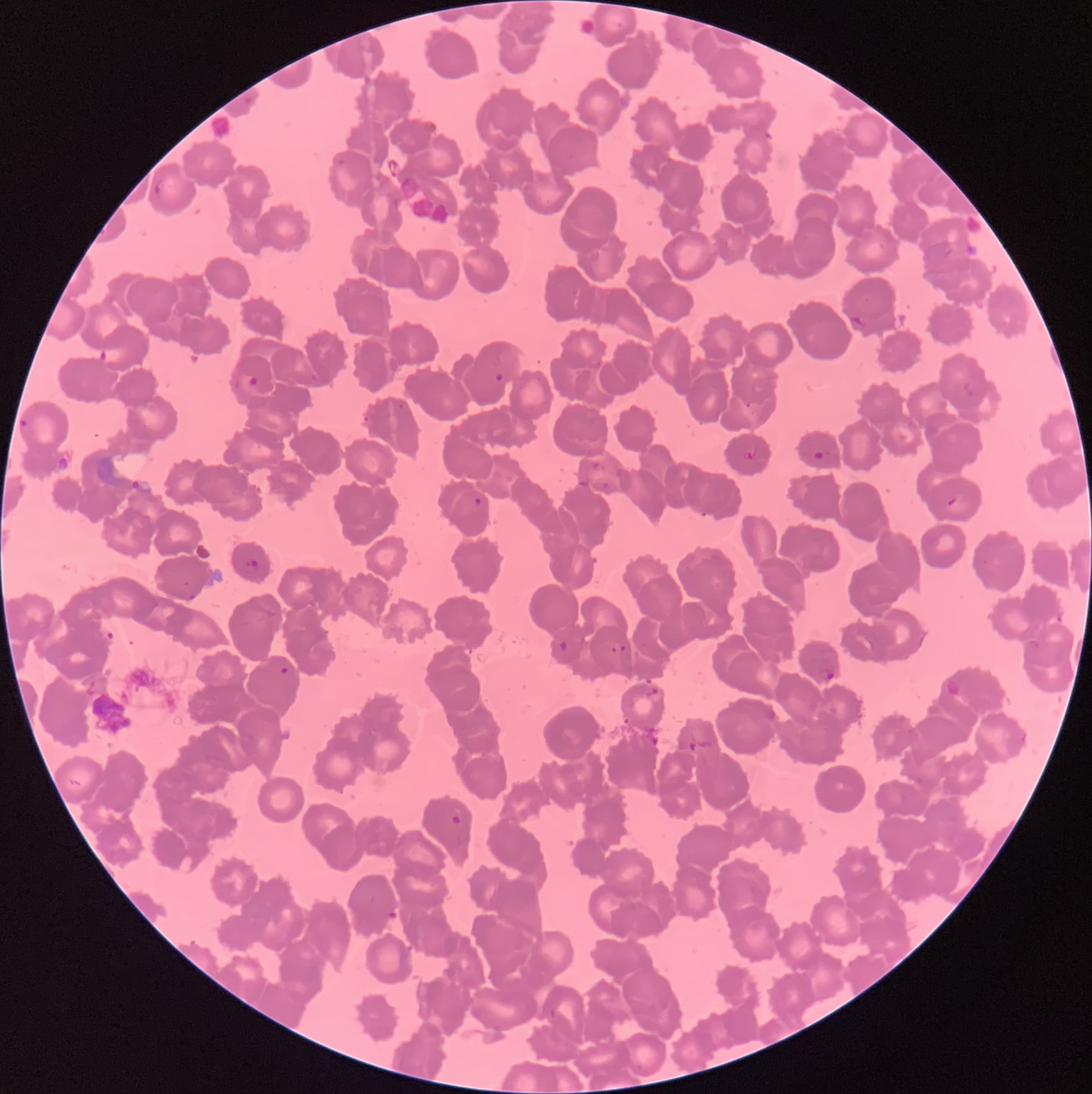

coordinate format = approximate bounding boxes as named x1/y1/x2/y2 corners in pixels
Plasmodium parasite locations = (x1=154, y1=177, x2=164, y2=198), (x1=849, y1=314, x2=867, y2=331), (x1=98, y1=345, x2=126, y2=365), (x1=493, y1=372, x2=505, y2=382), (x1=246, y1=374, x2=260, y2=387), (x1=963, y1=380, x2=976, y2=399), (x1=745, y1=401, x2=751, y2=409), (x1=362, y1=414, x2=372, y2=424), (x1=18, y1=418, x2=31, y2=430), (x1=743, y1=447, x2=757, y2=460), (x1=813, y1=449, x2=824, y2=460), (x1=592, y1=461, x2=606, y2=473), (x1=577, y1=478, x2=590, y2=488), (x1=129, y1=479, x2=143, y2=491), (x1=473, y1=496, x2=483, y2=506), (x1=945, y1=496, x2=958, y2=507), (x1=245, y1=558, x2=260, y2=570), (x1=188, y1=593, x2=197, y2=601), (x1=611, y1=640, x2=627, y2=653), (x1=1029, y1=640, x2=1041, y2=651), (x1=559, y1=641, x2=571, y2=652), (x1=280, y1=667, x2=290, y2=674), (x1=820, y1=668, x2=835, y2=682), (x1=644, y1=688, x2=659, y2=698), (x1=623, y1=716, x2=631, y2=724), (x1=688, y1=741, x2=708, y2=754), (x1=450, y1=814, x2=462, y2=826), (x1=548, y1=1009, x2=558, y2=1019)
Plasmodium parasites too small for a box (approximate object centers, named x/y in pixels) = (x=401, y=407)
red blood cell morphology = rouleaux formation
image size = 1092×1094 pixels
preparation = thin blood smear
modality = light microscopy